Identify the parasite.
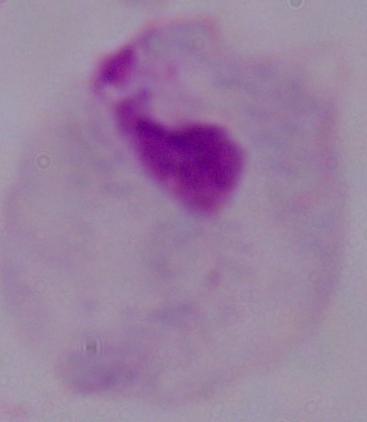
A trichomonad.

Photomicrograph. 1000x magnification.